Identify the parasite.
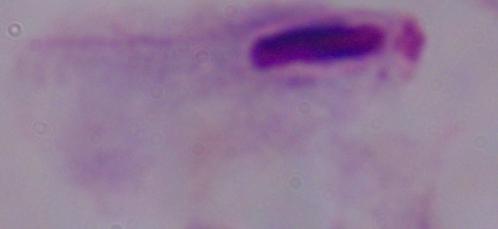
This is a trichomonad.

Micrograph. 1000x magnification.